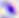
magnification = 400x
modality = photomicrograph
identification = Toxoplasma gondii